State the blood parasite species.
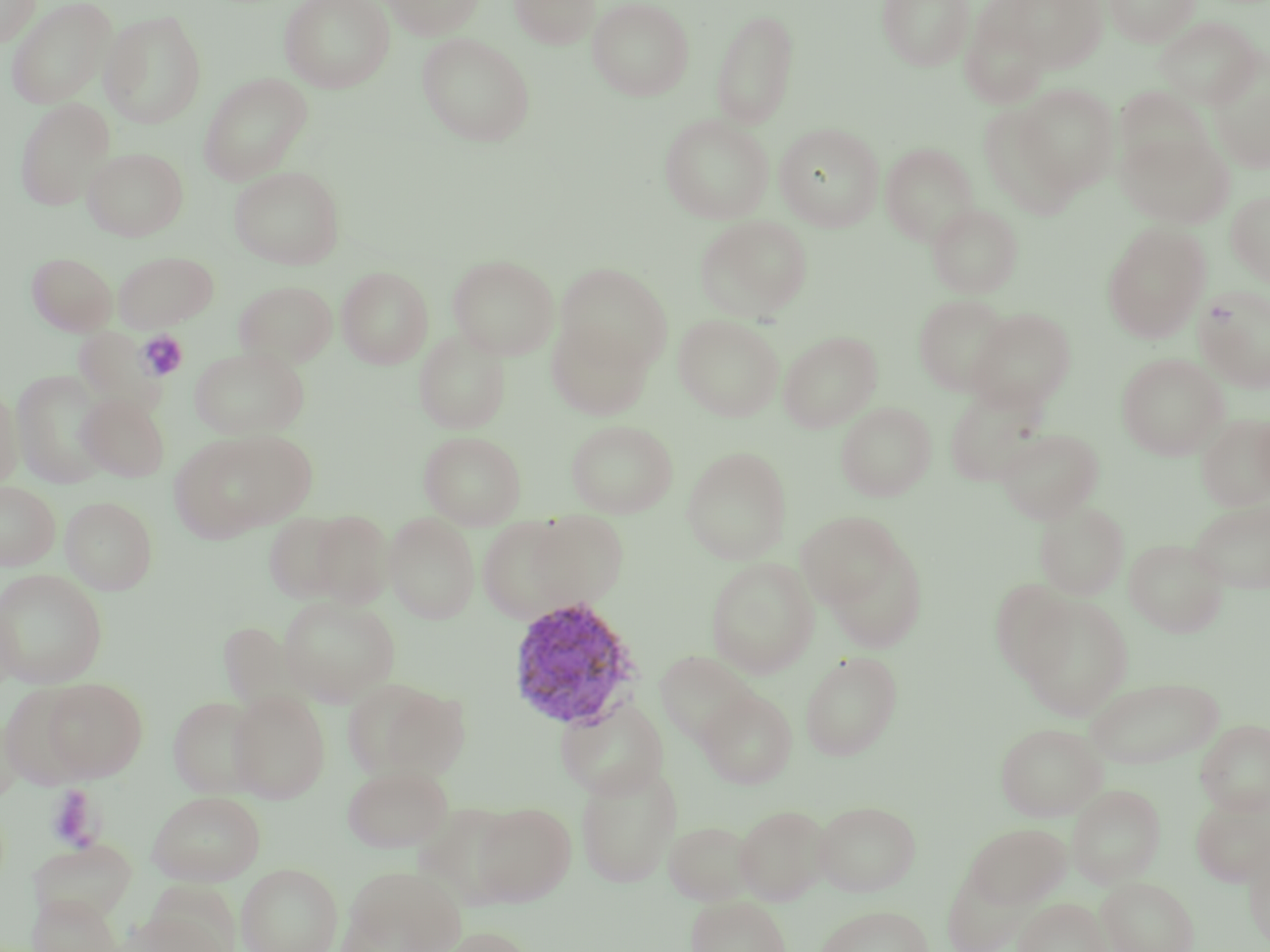

Plasmodium vivax.

Summary:
  - Coordinate format: approximate bounding boxes as named x1/y1/x2/y2 corners in pixels
  - Plasmodium vivax-infected red blood cell locations: (x1=506, y1=596, x2=644, y2=731)
  - Uninfected red blood cell locations: (x1=0, y1=0, x2=41, y2=47), (x1=6, y1=0, x2=117, y2=109), (x1=279, y1=0, x2=395, y2=92), (x1=382, y1=0, x2=486, y2=39), (x1=509, y1=0, x2=600, y2=49), (x1=587, y1=0, x2=695, y2=100), (x1=877, y1=0, x2=974, y2=70), (x1=1004, y1=0, x2=1108, y2=73), (x1=1104, y1=0, x2=1200, y2=46), (x1=711, y1=7, x2=800, y2=129), (x1=960, y1=8, x2=1051, y2=108), (x1=100, y1=10, x2=207, y2=129), (x1=1153, y1=16, x2=1264, y2=107), (x1=417, y1=32, x2=536, y2=146), (x1=1208, y1=63, x2=1270, y2=173), (x1=199, y1=72, x2=312, y2=184), (x1=1013, y1=83, x2=1120, y2=195), (x1=1114, y1=87, x2=1212, y2=178), (x1=15, y1=98, x2=115, y2=211), (x1=978, y1=103, x2=1081, y2=219), (x1=659, y1=114, x2=774, y2=224), (x1=775, y1=122, x2=884, y2=231), (x1=1117, y1=129, x2=1235, y2=227), (x1=880, y1=143, x2=978, y2=246), (x1=82, y1=147, x2=188, y2=241), (x1=229, y1=165, x2=345, y2=269), (x1=1226, y1=190, x2=1270, y2=287), (x1=927, y1=203, x2=1023, y2=298), (x1=695, y1=215, x2=813, y2=322), (x1=1102, y1=222, x2=1211, y2=343), (x1=113, y1=251, x2=218, y2=331), (x1=27, y1=252, x2=117, y2=336), (x1=447, y1=254, x2=559, y2=359), (x1=555, y1=262, x2=672, y2=373), (x1=337, y1=266, x2=433, y2=368), (x1=235, y1=280, x2=337, y2=368), (x1=1194, y1=285, x2=1270, y2=393), (x1=914, y1=294, x2=1013, y2=396), (x1=969, y1=307, x2=1076, y2=411), (x1=674, y1=314, x2=784, y2=421), (x1=547, y1=319, x2=653, y2=420), (x1=74, y1=328, x2=166, y2=413), (x1=414, y1=330, x2=510, y2=434), (x1=778, y1=330, x2=883, y2=432), (x1=190, y1=346, x2=309, y2=440), (x1=1116, y1=353, x2=1229, y2=460), (x1=12, y1=371, x2=113, y2=487), (x1=0, y1=385, x2=24, y2=491), (x1=944, y1=385, x2=1049, y2=486), (x1=77, y1=393, x2=170, y2=482), (x1=836, y1=401, x2=936, y2=501), (x1=1253, y1=410, x2=1270, y2=503), (x1=1197, y1=413, x2=1270, y2=511), (x1=566, y1=419, x2=678, y2=518), (x1=996, y1=427, x2=1103, y2=523), (x1=170, y1=430, x2=311, y2=540), (x1=419, y1=431, x2=526, y2=529), (x1=681, y1=446, x2=792, y2=564), (x1=0, y1=481, x2=60, y2=570), (x1=60, y1=496, x2=157, y2=595), (x1=1188, y1=497, x2=1270, y2=594), (x1=1034, y1=499, x2=1130, y2=600), (x1=305, y1=509, x2=395, y2=608), (x1=263, y1=511, x2=360, y2=604), (x1=522, y1=511, x2=630, y2=611), (x1=796, y1=511, x2=907, y2=612), (x1=384, y1=512, x2=480, y2=624), (x1=476, y1=515, x2=590, y2=624), (x1=821, y1=535, x2=929, y2=654), (x1=1124, y1=538, x2=1229, y2=637), (x1=705, y1=556, x2=819, y2=678), (x1=0, y1=569, x2=107, y2=688), (x1=989, y1=579, x2=1078, y2=683), (x1=1015, y1=593, x2=1134, y2=719), (x1=278, y1=595, x2=401, y2=706), (x1=216, y1=622, x2=304, y2=710), (x1=654, y1=650, x2=757, y2=748), (x1=800, y1=652, x2=903, y2=760), (x1=39, y1=677, x2=148, y2=781), (x1=343, y1=677, x2=470, y2=783), (x1=1085, y1=677, x2=1224, y2=768), (x1=1, y1=683, x2=94, y2=790), (x1=697, y1=688, x2=798, y2=789), (x1=228, y1=690, x2=331, y2=803), (x1=168, y1=695, x2=265, y2=798), (x1=555, y1=695, x2=668, y2=800), (x1=0, y1=709, x2=22, y2=804), (x1=1196, y1=719, x2=1270, y2=815), (x1=995, y1=721, x2=1106, y2=821), (x1=575, y1=761, x2=682, y2=888), (x1=342, y1=764, x2=452, y2=853), (x1=1067, y1=784, x2=1166, y2=888), (x1=148, y1=791, x2=265, y2=885), (x1=1190, y1=794, x2=1270, y2=887), (x1=813, y1=800, x2=922, y2=896), (x1=473, y1=802, x2=575, y2=906), (x1=734, y1=804, x2=832, y2=905), (x1=663, y1=820, x2=756, y2=906), (x1=964, y1=822, x2=1070, y2=908), (x1=1244, y1=833, x2=1270, y2=948), (x1=28, y1=837, x2=138, y2=926), (x1=237, y1=862, x2=343, y2=952), (x1=337, y1=865, x2=466, y2=952), (x1=942, y1=866, x2=1027, y2=952), (x1=1097, y1=877, x2=1198, y2=952), (x1=27, y1=891, x2=121, y2=952), (x1=686, y1=895, x2=791, y2=952), (x1=1014, y1=897, x2=1111, y2=952), (x1=814, y1=904, x2=934, y2=952), (x1=122, y1=906, x2=233, y2=952), (x1=432, y1=925, x2=538, y2=952)
  - Platelet locations: (x1=137, y1=331, x2=189, y2=381), (x1=45, y1=786, x2=100, y2=850)
  - Magnification: 1000x
  - Modality: optical microscopy
  - Image size: 1270×952 pixels
  - Preparation: thin blood film
  - Stain: May-Grünwald-Giemsa
  - Field of view: one of a larger specimen